Classify this cell by malaria status.
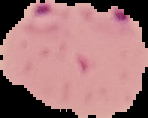

Parasitized.

{
  "image_size": "148×118 pixels",
  "image_type": "cell region segmented out of the field of view; surrounding area masked to black",
  "preparation": "thin blood smear"
}